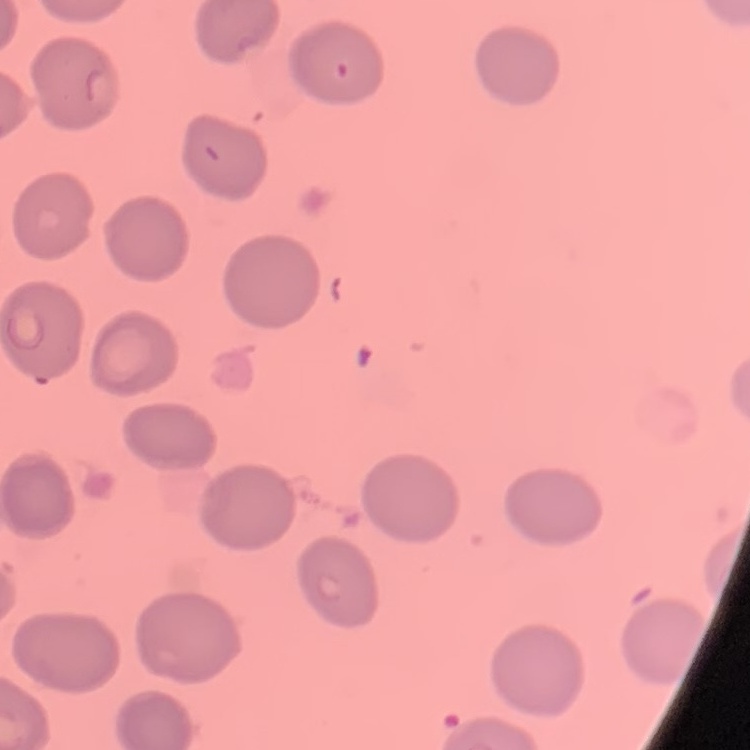

Summary:
  - Red blood cell morphology: no rouleaux formation
  - Preparation: thin peripheral smear
  - Image type: one tile cut from a larger photomicrograph
  - Stain: Field's or Giemsa